State which parasite is depicted.
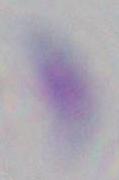
Toxoplasma gondii.

1000x magnification. Micrograph.